Identify the preparation type.
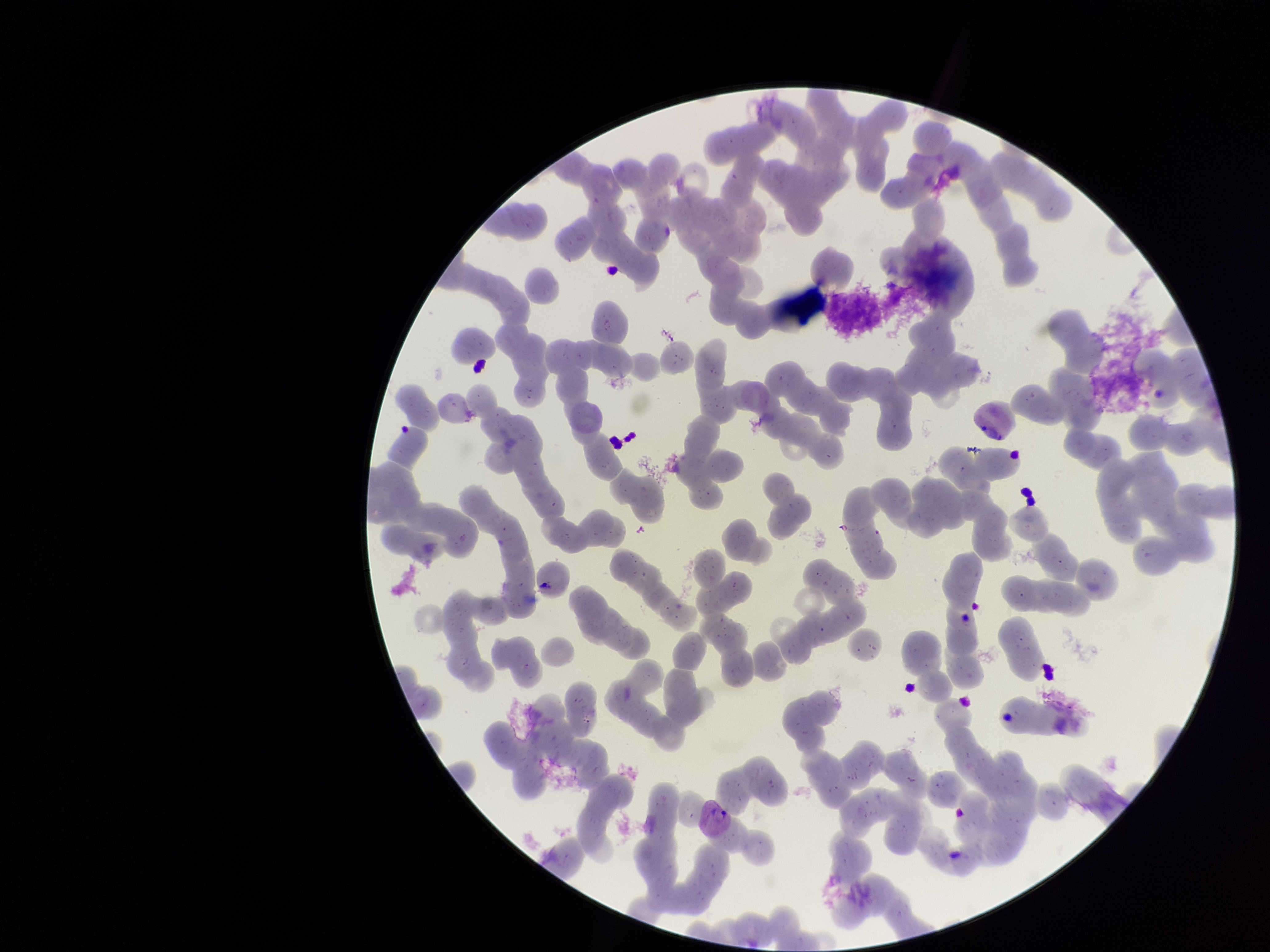
A thin smear.

parasitized red blood cells = none identified
parasitized red blood cell count = 0
capture = smartphone photograph through the microscope eyepiece
patient malaria status = positive
stain = Giemsa
image size = 1270×952 pixels
species reported for this patient = Plasmodium vivax
red blood cell count = 197
field of view = one from this slide